Locate every Plasmodium parasite and every leukocyte.
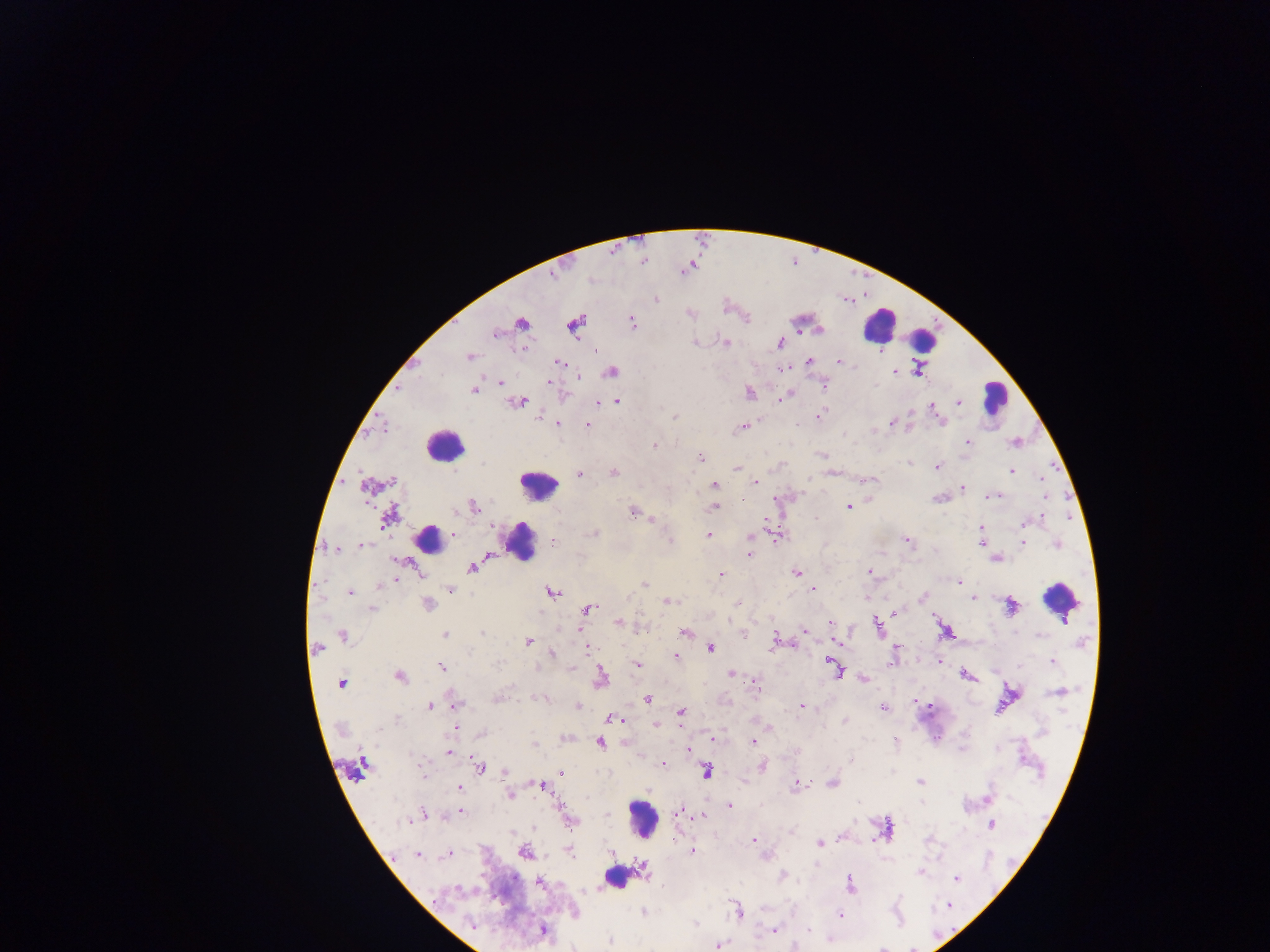

Approximate centers as x y in pixels.
Plasmodium parasites: 656 299; 632 322; 521 324; 574 325; 495 333; 725 342; 693 343; 779 343; 596 351; 470 356; 808 362; 839 362; 559 363; 916 371; 611 372; 894 372; 501 382; 549 382; 824 385; 474 390; 749 393; 785 396; 617 401; 519 402; 598 403; 958 403; 933 408; 819 416; 539 417; 674 418; 893 422; 941 422; 558 424; 588 424; 741 427; 967 442; 654 445; 701 458; 937 467; 736 468; 1011 470; 614 473; 579 475; 1043 477; 872 480; 756 482; 714 485; 962 488; 993 496; 1045 497; 848 506; 474 507; 715 508; 455 511; 633 512; 389 517; 816 518; 653 520; 1024 523; 981 528; 454 533; 594 533; 708 535; 751 536; 670 540; 907 541; 981 541; 553 543; 1023 543; 1056 544; 361 545; 334 548; 750 554; 996 559; 472 567; 796 572; 869 572; 722 574; 396 580; 959 582; 379 585; 644 585; 450 589; 813 589; 350 592; 551 592; 629 596; 923 596; 972 598; 668 601; 738 603; 428 604; 1012 607; 588 608; 372 609; 894 612; 619 622; 831 623; 878 626; 809 628; 804 630; 945 631; 685 632; 743 633; 482 634; 445 635; 1040 635; 344 637; 528 642; 774 642; 837 643; 587 647; 711 648; 318 649; 895 649; 552 654; 676 656; 939 662; 1052 662; 637 664; 442 667; 572 668; 835 669; 732 674; 966 675; 399 676; 601 677; 754 680; 863 680; 340 683; 1059 692; 497 698; 543 698; 647 699; 916 701; 456 705; 577 705; 801 706; 430 707; 883 708; 681 712; 613 718; 398 720; 845 721; 657 725; 456 727; 481 733; 713 738; 895 740; 753 742; 600 743; 534 745; 688 750; 449 752; 851 760; 662 763; 479 766; 762 766; 421 769; 561 772; 706 772; 505 773; 920 781; 832 782; 542 786; 798 786; 460 788; 510 796; 988 797; 729 806; 461 811; 679 812; 422 815; 607 815; 703 816; 415 818; 409 821; 569 821; 991 824; 512 832; 792 832; 754 840; 674 841; 819 843; 692 851; 610 852; 525 853; 570 853; 447 855; 418 856; 816 865; 643 868; 920 872; 782 876; 956 879; 540 882; 850 884; 457 889; 949 905; 738 911; 643 912; 841 915; 472 924; 694 924; 809 929; 543 930; 774 930; 610 941; 718 946; 881 948.
Leukocytes: 879 325; 922 339; 995 396; 444 445; 539 485; 429 538; 521 543; 1060 600; 643 819; 618 878.

Mobile-phone photograph taken through the microscope. Image is 1270×952 pixels. Sample from Ghana. Thick blood smear. Single field of view.